Report the malaria status of this cell.
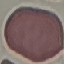

Uninfected.

Summary:
  - Capture: smartphone camera at the microscope eyepiece
  - Preparation: thin blood film
  - Image type: cell patch, automatically extracted from a larger field of view and resized to 64 × 64 pixels
  - Stain: Giemsa